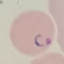

Summary:
  - Result: malaria parasites identified
  - Capture: smartphone camera at the microscope eyepiece
  - Preparation: thin blood smear
  - Stain: Giemsa
  - Image type: cell patch, automatically extracted from a larger field of view and resized to 64 × 64 pixels